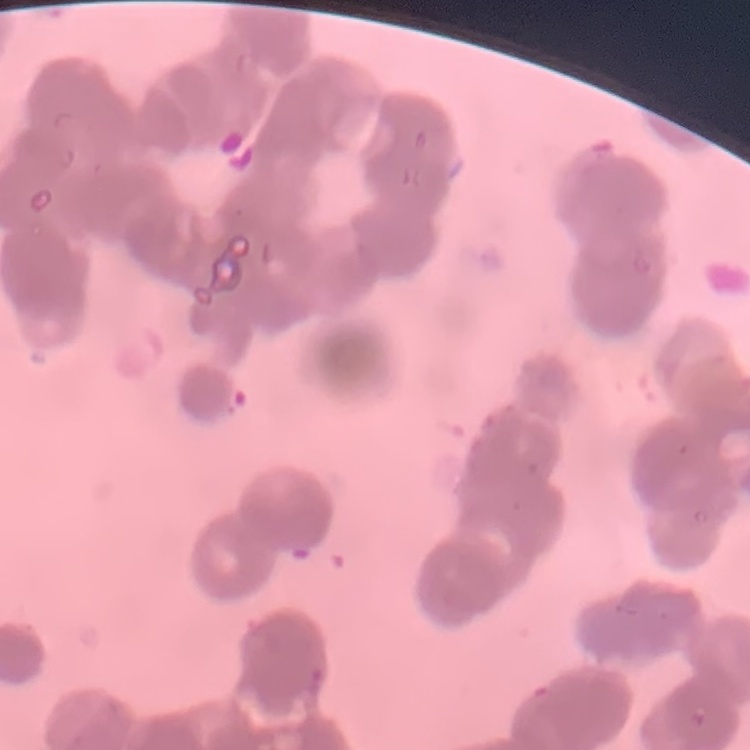

The erythrocytes show rouleaux formation. Thin peripheral smear. One tile cut from a larger photomicrograph. Field's or Giemsa stain.